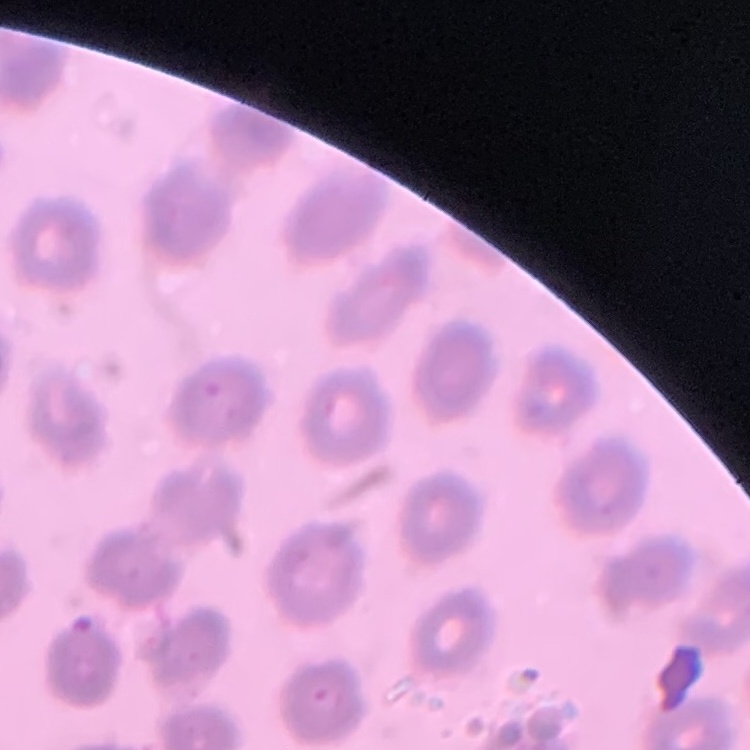
Summary:
  - Erythrocyte morphology: no rouleaux formation
  - Image type: one tile cut from a larger photomicrograph
  - Stain: Field's or Giemsa
  - Preparation: thin blood smear